Identify the cell.
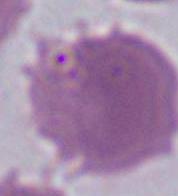

This is an erythrocyte.

Summary:
  - Magnification: 1000x
  - Modality: photomicrograph